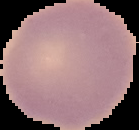
result = no Plasmodium parasites seen
image size = 139×130 pixels
image type = cell region segmented out of the field of view; surrounding area masked to black
preparation = thin blood film